Name the parasite shown.
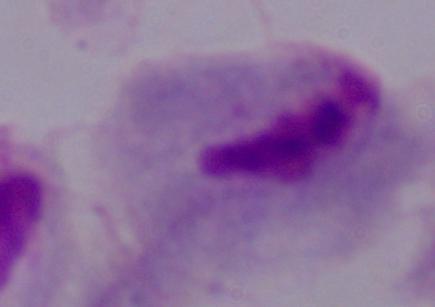

A trichomonad.

modality = micrograph
magnification = 1000x